Outline each blood parasite and name the species.
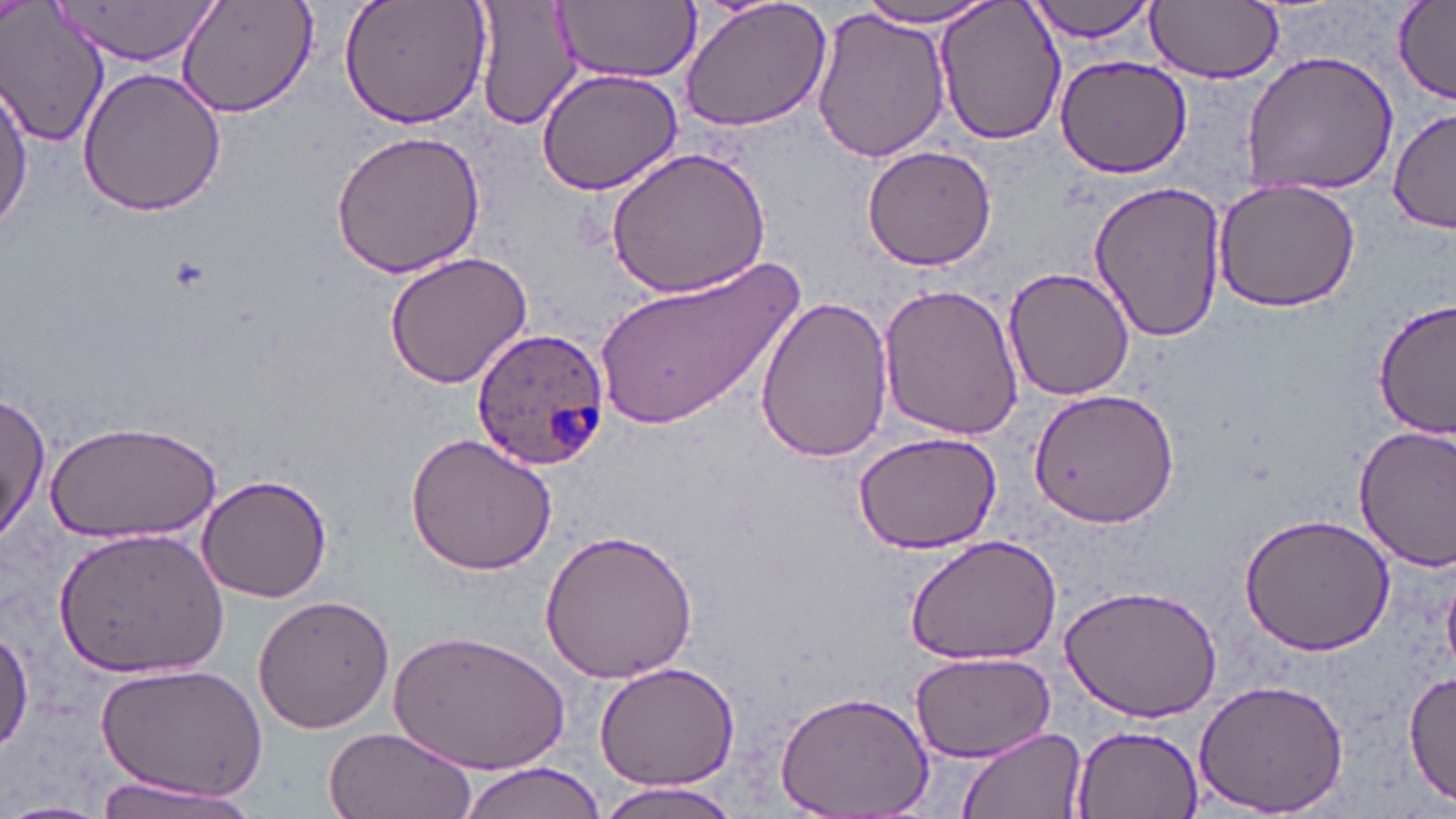

Approximate bounding boxes as (x1,y1)-(x2,y2) corner pairs in pixels.
Plasmodium ovale-infected red blood cells: (470,326)-(609,472).
No Plasmodium falciparum, Plasmodium malariae, Plasmodium vivax, Babesia divergens, or Trypanosoma brucei observed.

Uninfected red blood cell locations: (0,0)-(110,148), (51,0)-(218,68), (174,0)-(322,119), (339,0)-(490,127), (472,0)-(585,132), (678,0)-(831,132), (933,0)-(1067,147), (1024,0)-(1162,44), (1148,0)-(1283,85), (552,1)-(701,84), (852,2)-(1000,29), (1392,2)-(1453,104), (810,7)-(951,165), (1240,48)-(1398,196), (1052,54)-(1196,177), (534,65)-(685,195), (76,67)-(228,217), (0,78)-(34,239), (1388,107)-(1454,237), (329,129)-(487,280), (862,144)-(997,272), (605,146)-(774,299), (1211,178)-(1361,312), (1089,180)-(1228,343), (382,251)-(534,390), (593,252)-(805,432), (1003,266)-(1134,401), (877,282)-(1025,441), (756,295)-(895,462), (1375,298)-(1456,437), (1026,388)-(1178,527), (0,393)-(50,544), (46,420)-(223,543), (1354,424)-(1456,571), (852,430)-(1002,554), (405,435)-(558,577), (195,475)-(334,604), (1238,511)-(1397,658), (51,525)-(228,678), (539,528)-(698,684), (904,534)-(1062,664), (1060,582)-(1223,723), (251,594)-(396,733), (0,622)-(31,753), (392,628)-(569,773), (908,651)-(1059,765), (96,661)-(267,801), (594,662)-(740,790), (1405,668)-(1456,808), (1193,678)-(1350,815), (774,690)-(935,817), (1071,725)-(1203,819), (957,726)-(1086,818), (326,728)-(476,819), (455,760)-(610,819), (86,773)-(263,819), (589,780)-(747,819), (0,800)-(115,819). Slide-level diagnosis: Plasmodium ovale. Image is 1456×819 pixels. May-Grünwald-Giemsa stain. Thin blood smear. 1000x magnification. Single field of view. Light microscopy.